Assess the morphology of the red blood cells.
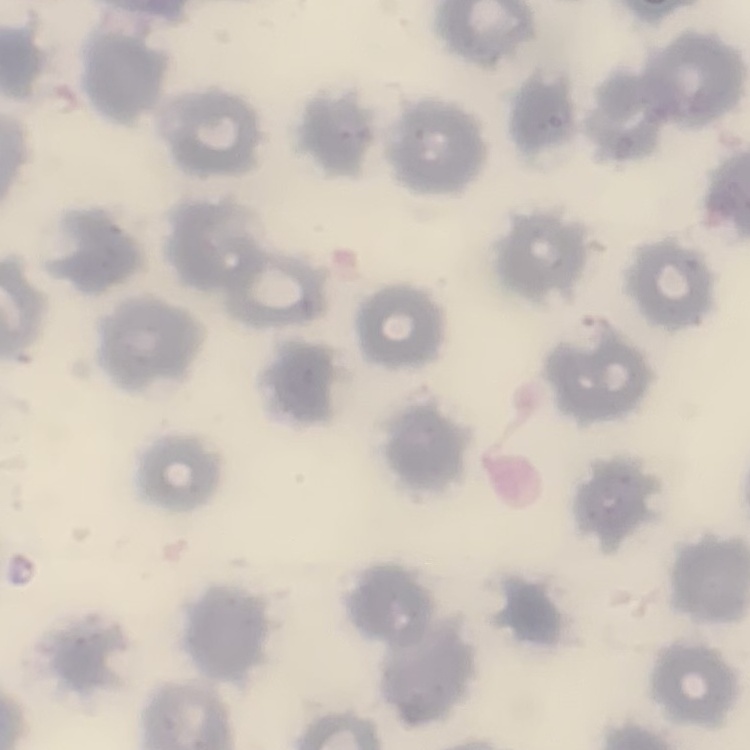
No rouleaux formation.

Thin blood film. Field's or Giemsa stain. Square crop of a larger photomicrograph.